Describe the morphology of the red blood cells.
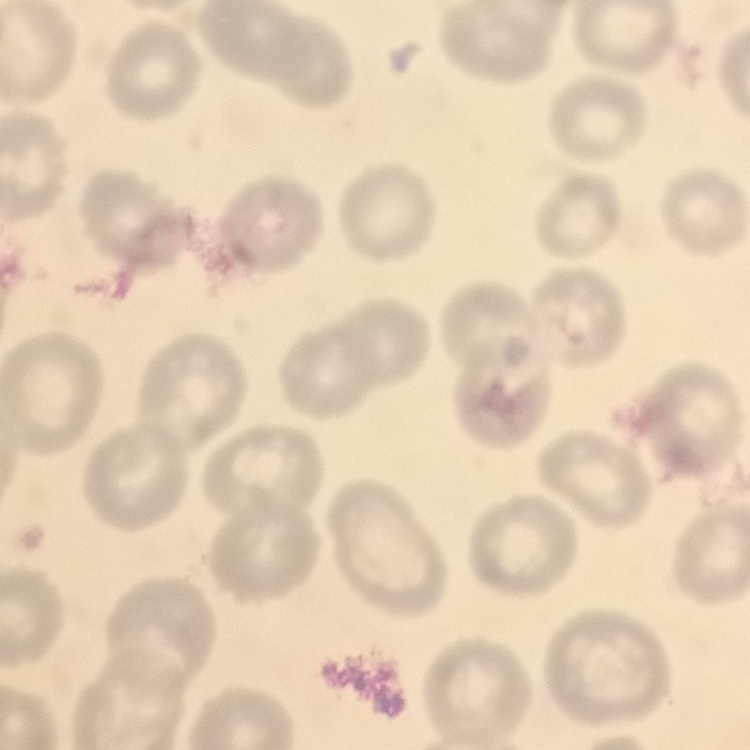
They show no rouleaux formation.

{
  "stain": "Field's or Giemsa",
  "image_type": "square crop of a larger photomicrograph",
  "preparation": "thin blood film"
}